Classify this cell by malaria status.
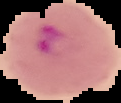
Parasitized.

preparation = thin blood smear
image type = cell region segmented out of the field of view; surrounding area masked to black
image size = 121×103 pixels